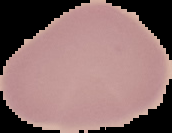
image type = segmented cell region with the area outside set to black
image size = 172×133 pixels
result = no malaria parasites detected
preparation = thin blood smear